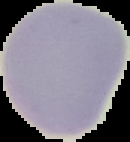
Summary:
  - Result: no malaria parasites detected
  - Image type: segmented cell region with the area outside set to black
  - Preparation: thin blood film
  - Image size: 130×142 pixels